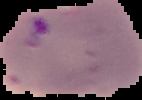
Summary:
  - Malaria status: parasitized
  - Image type: segmented cell region with the area outside set to black
  - Preparation: thin blood film
  - Image size: 142×100 pixels